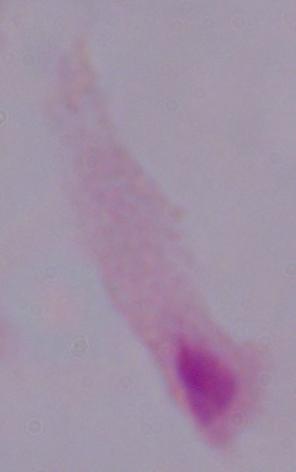
{
  "magnification": "1000x",
  "modality": "micrograph",
  "identification": "trichomonad"
}